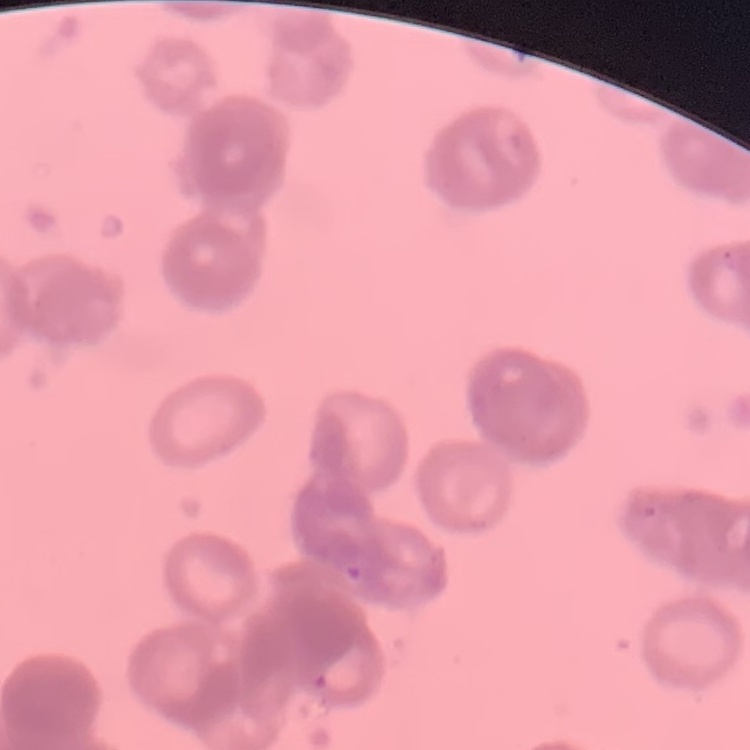

The red blood cells show rouleaux formation. One tile cut from a larger photomicrograph. Thin blood film. Stained with either Field's or Giemsa.